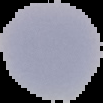
From a thin blood film. Result: no Plasmodium parasites seen. Cell region segmented out of the field of view; the surrounding area is masked to black. Image is 103×103 pixels.